Classify this cell by malaria status.
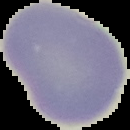

Uninfected.

Summary:
  - Image size: 130×130 pixels
  - Image type: segmented cell region with the area outside set to black
  - Preparation: thin blood smear